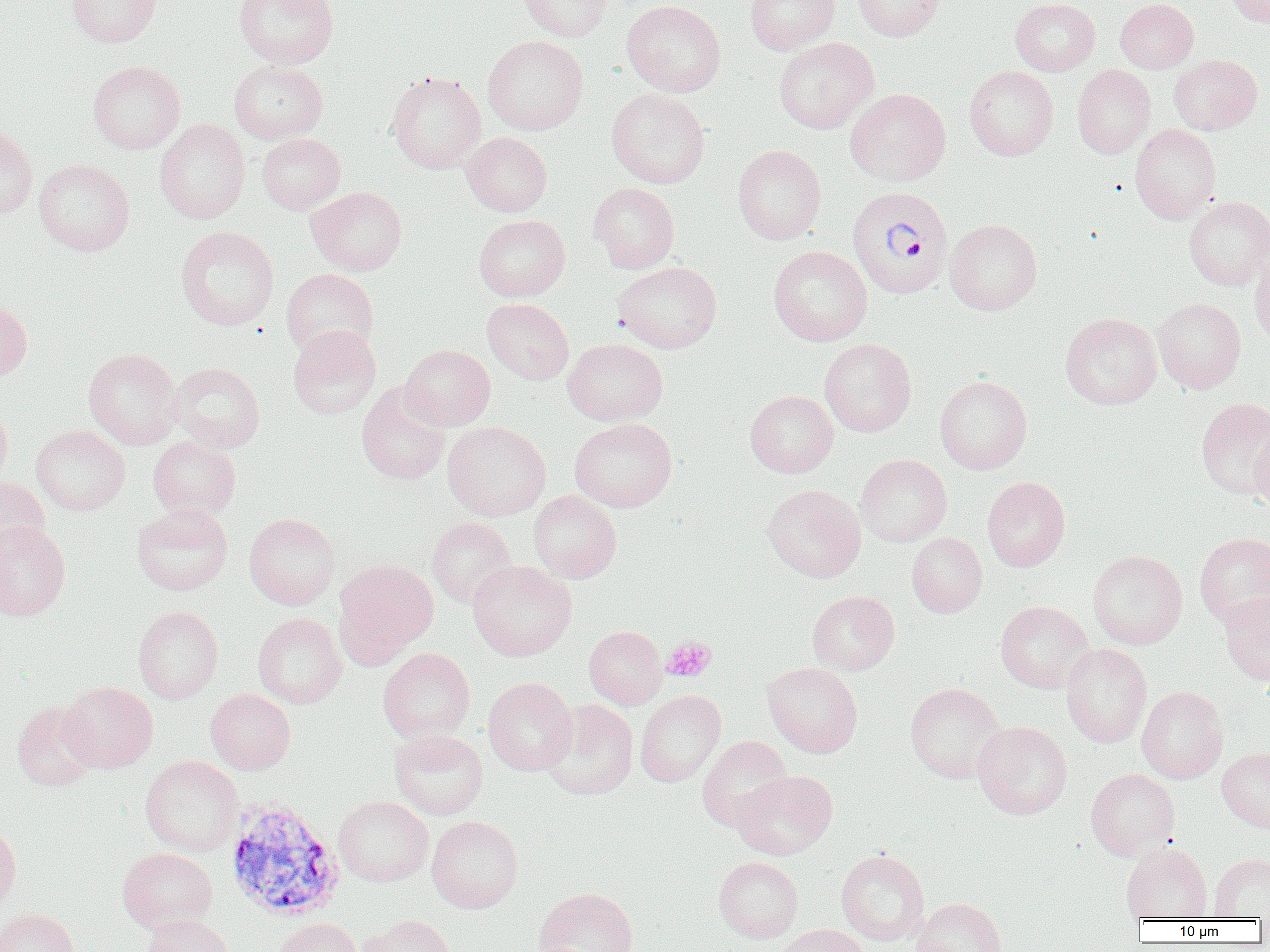

slide-level diagnosis = Plasmodium vivax
platelet locations = approximate bounding boxes as (x1, y1, x2, y2) in pixels: (661, 637, 716, 682)
modality = optical microscopy
field of view = single
Plasmodium vivax-infected red blood cell locations = approximate bounding boxes as (x1, y1, x2, y2) in pixels: (847, 185, 953, 299), (224, 799, 344, 921)
image size = 1270×952 pixels
magnification = 1000x
preparation = thin blood smear
uninfected red blood cell locations = approximate bounding boxes as (x1, y1, x2, y2) in pixels: (65, 0, 162, 47), (234, 0, 339, 68), (519, 0, 614, 42), (622, 0, 726, 97), (744, 0, 840, 54), (852, 0, 946, 41), (1010, 0, 1100, 75), (1115, 0, 1198, 73), (1228, 0, 1269, 27), (482, 35, 588, 135), (774, 37, 879, 134), (1169, 54, 1262, 135), (88, 60, 186, 154), (229, 60, 328, 144), (1071, 64, 1156, 159), (964, 66, 1058, 161), (386, 71, 486, 174), (606, 88, 710, 189), (845, 88, 951, 185), (154, 118, 251, 224), (1130, 124, 1221, 223), (0, 125, 37, 218), (461, 132, 552, 216), (257, 133, 346, 215), (732, 144, 826, 244), (34, 158, 134, 256), (588, 183, 679, 273), (307, 187, 407, 275), (1183, 196, 1270, 290), (473, 214, 570, 301), (945, 218, 1042, 315), (175, 226, 280, 330), (768, 246, 872, 346), (1250, 250, 1270, 347), (612, 261, 722, 353), (281, 268, 379, 359), (482, 298, 574, 385), (1153, 298, 1246, 394), (0, 299, 32, 382), (1060, 312, 1161, 410), (287, 325, 381, 419), (562, 338, 667, 425), (819, 338, 916, 437), (400, 344, 495, 430), (84, 348, 182, 449), (168, 361, 265, 453), (934, 375, 1032, 474), (356, 383, 450, 485), (744, 390, 839, 478), (1196, 397, 1270, 501), (0, 403, 12, 491), (569, 418, 677, 512), (442, 420, 551, 521), (31, 425, 130, 515), (1250, 427, 1270, 511), (147, 436, 241, 519), (855, 454, 952, 547), (982, 476, 1070, 571), (0, 477, 50, 564), (761, 484, 866, 583), (528, 490, 622, 583), (131, 503, 233, 596), (244, 513, 339, 610), (426, 517, 517, 609), (0, 520, 71, 621), (907, 532, 987, 617), (1194, 532, 1270, 627), (1088, 550, 1187, 649), (334, 559, 439, 666), (468, 560, 577, 661), (807, 591, 900, 676), (1219, 591, 1270, 686), (995, 600, 1094, 694), (133, 606, 223, 703), (252, 613, 346, 708), (583, 625, 667, 709), (1060, 644, 1152, 748), (377, 648, 475, 742), (763, 662, 863, 758), (483, 677, 577, 775), (59, 681, 158, 773), (905, 682, 1007, 783), (1136, 686, 1228, 783), (205, 689, 295, 774), (635, 690, 726, 787), (541, 699, 638, 800), (12, 701, 101, 791), (973, 721, 1072, 820), (390, 729, 488, 820), (696, 735, 793, 832), (1217, 747, 1270, 833), (140, 755, 243, 856), (1085, 768, 1180, 860), (732, 769, 837, 860), (334, 796, 433, 887), (426, 815, 523, 913), (0, 823, 21, 914), (1120, 843, 1212, 921), (118, 847, 217, 933), (836, 849, 929, 945), (1209, 855, 1270, 920), (714, 856, 803, 943), (533, 887, 639, 952), (912, 897, 1007, 952), (0, 908, 79, 952), (143, 915, 234, 952), (358, 915, 456, 952), (273, 918, 362, 952), (776, 924, 870, 952)